Report the malaria status of this cell.
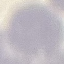
It is uninfected.

preparation = thin smear
stain = Giemsa
capture = smartphone camera at the microscope eyepiece
image type = cell patch, automatically extracted from a larger field of view and resized to 64 × 64 pixels